Locate platelets.
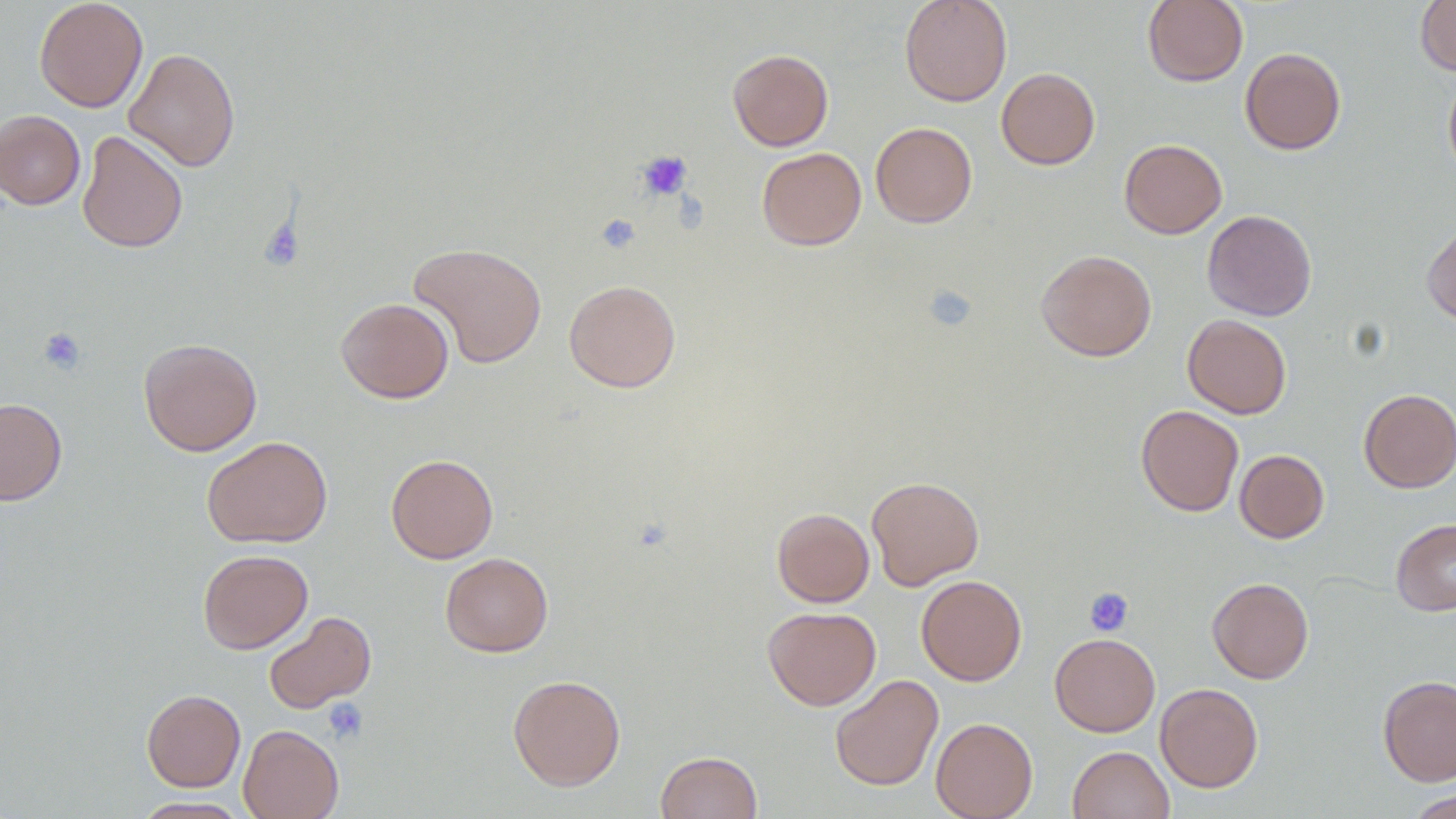
Approximate bounding boxes as (x1, y1, x2, y2) in pixels.
Platelets: (635, 150, 693, 202), (677, 189, 714, 234), (595, 213, 640, 254), (258, 216, 304, 272), (921, 284, 978, 333), (38, 326, 86, 375), (1084, 587, 1134, 636), (322, 697, 368, 745).

Summary:
  - Uninfected red blood cell locations: (34, 0, 148, 112), (899, 0, 1012, 107), (1142, 0, 1249, 87), (1415, 0, 1456, 76), (123, 47, 241, 172), (1240, 47, 1346, 155), (728, 48, 834, 151), (996, 67, 1100, 170), (1443, 71, 1456, 182), (0, 110, 85, 209), (870, 122, 977, 228), (77, 130, 188, 253), (1119, 138, 1227, 238), (756, 147, 867, 250), (1202, 210, 1317, 321), (1422, 221, 1456, 326), (408, 242, 548, 368), (1036, 249, 1157, 361), (564, 279, 681, 392), (336, 297, 454, 403), (1182, 314, 1292, 419), (138, 338, 262, 456), (1358, 388, 1456, 493), (0, 397, 67, 505), (1136, 405, 1244, 516), (202, 435, 333, 548), (1235, 449, 1329, 543), (386, 454, 499, 563), (866, 476, 984, 590), (772, 508, 874, 607), (1391, 517, 1456, 616), (197, 549, 313, 654), (440, 552, 553, 657), (916, 575, 1027, 686), (1207, 577, 1314, 684), (763, 606, 881, 710), (263, 611, 376, 714), (1049, 633, 1160, 736), (507, 674, 626, 791), (829, 674, 944, 791), (1377, 675, 1456, 786), (1155, 683, 1263, 792), (141, 689, 246, 792), (930, 717, 1038, 819), (238, 724, 344, 819), (1068, 745, 1174, 819), (655, 751, 762, 819), (1404, 788, 1456, 818), (129, 796, 253, 818)
  - Slide-level diagnosis: no evidence of blood parasites
  - Modality: light microscopy
  - Preparation: thin blood film
  - Magnification: 1000x
  - Field of view: single
  - Image size: 1456×819 pixels